Point out each Plasmodium parasite.
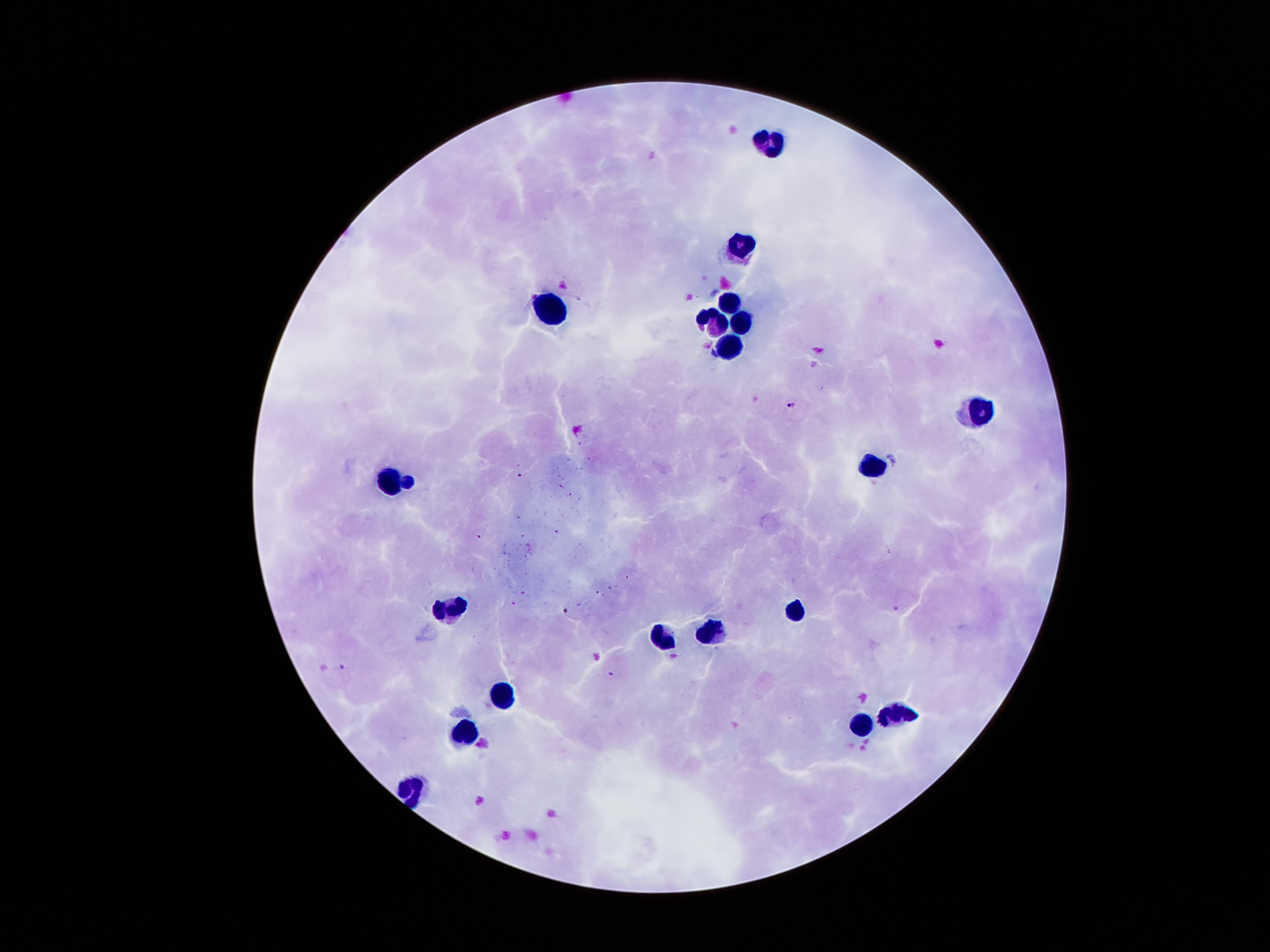
Approximate centers as (x, y) in pixels.
Plasmodium parasites: (562, 285), (707, 345), (790, 404), (896, 608), (342, 665), (610, 674).

field_of_view: single
preparation: thick peripheral-blood smear
magnification: 100x
leukocyte_locations: 'approximate centers as (x, y) in pixels: (771, 145), (739, 248), (729, 301), (553, 312), (715, 320), (742, 322), (728, 353), (972, 411), (870, 466), (387, 476), (409, 484), (444, 606), (790, 613), (709, 635), (655, 639), (500, 693), (897, 716), (862, 726), (462, 736), (410, 790)'
capture: smartphone through the microscope eyepiece
image_size: 1270×952 pixels
patient_malaria_status: infected with Plasmodium falciparum
stain: Giemsa